State the blood parasite species.
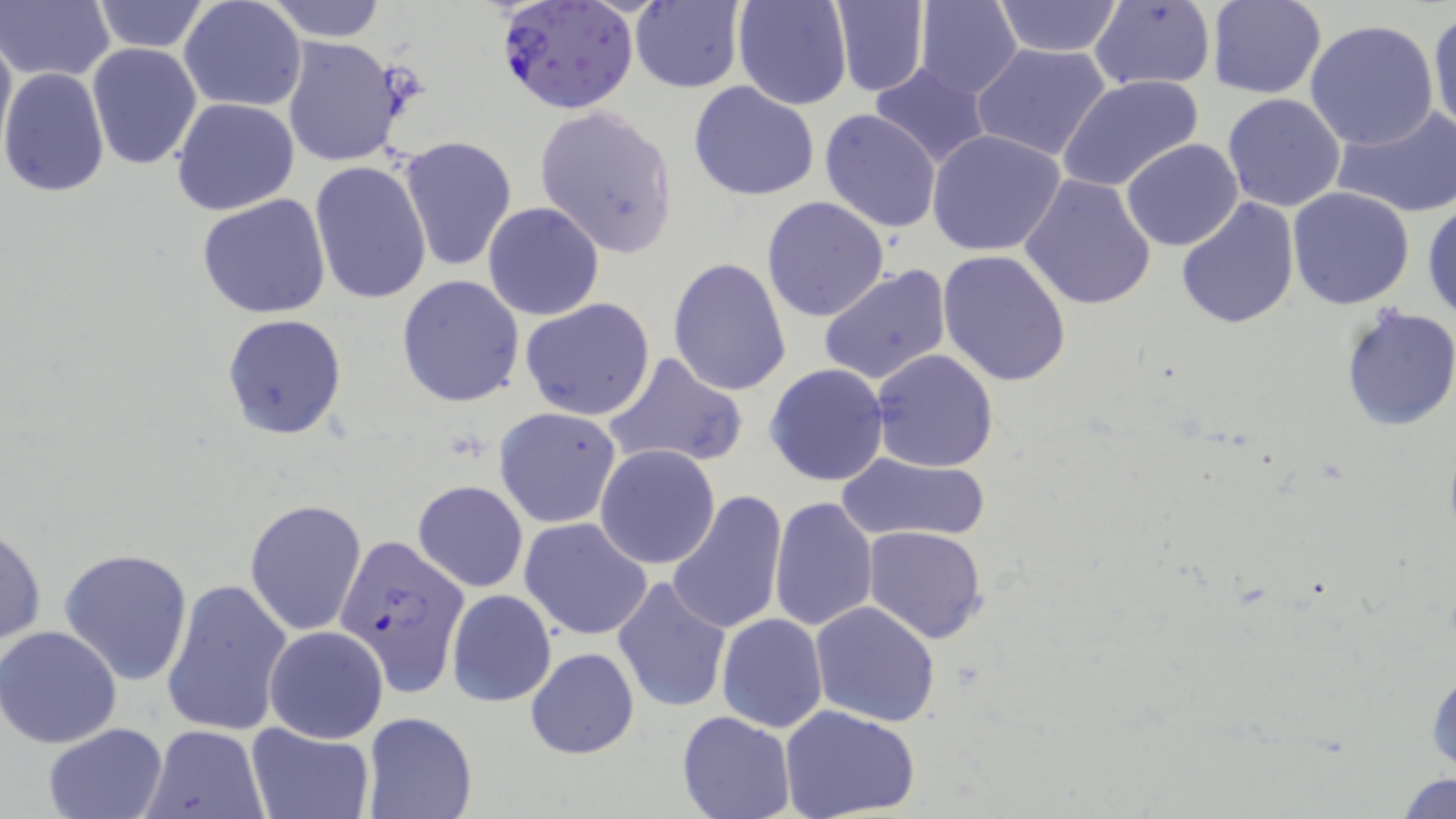

Plasmodium falciparum.

Summary:
  - Coordinate format: approximate bounding boxes as [x1, y1, x2, y2] in pixels
  - Plasmodium falciparum-infected red blood cell locations: [495, 0, 641, 116], [334, 537, 470, 700]
  - Uninfected red blood cell locations: [88, 0, 213, 54], [178, 0, 307, 112], [261, 0, 389, 41], [731, 0, 852, 109], [913, 0, 1022, 98], [630, 1, 745, 93], [831, 1, 931, 95], [992, 1, 1124, 56], [1205, 1, 1328, 100], [1, 2, 114, 83], [1087, 2, 1217, 91], [854, 3, 1008, 139], [1428, 8, 1456, 139], [1302, 19, 1439, 152], [0, 23, 15, 160], [281, 35, 414, 168], [86, 42, 203, 171], [970, 43, 1114, 163], [869, 62, 991, 167], [0, 66, 112, 197], [1057, 74, 1205, 193], [688, 82, 821, 201], [1221, 91, 1346, 211], [170, 97, 299, 215], [533, 104, 679, 258], [1331, 106, 1456, 219], [819, 108, 942, 231], [927, 129, 1066, 256], [397, 135, 517, 272], [1121, 139, 1245, 252], [308, 161, 432, 305], [1020, 174, 1157, 309], [1286, 187, 1415, 311], [197, 194, 333, 318], [761, 196, 889, 323], [1175, 196, 1301, 331], [1422, 198, 1456, 324], [482, 200, 604, 321], [938, 251, 1072, 388], [667, 257, 793, 397], [818, 266, 952, 388], [397, 274, 524, 407], [520, 298, 655, 422], [1339, 307, 1456, 432], [221, 313, 347, 440], [870, 348, 999, 472], [602, 350, 749, 471], [764, 363, 890, 486], [494, 407, 622, 528], [595, 444, 720, 569], [836, 451, 992, 544], [413, 480, 528, 593], [665, 490, 786, 635], [769, 495, 879, 632], [245, 498, 367, 636], [520, 517, 654, 640], [0, 522, 46, 651], [863, 527, 986, 644], [58, 547, 195, 686], [612, 575, 732, 714], [162, 577, 293, 739], [446, 589, 556, 707], [809, 600, 940, 727], [717, 614, 827, 731], [0, 626, 122, 748], [264, 626, 388, 743], [524, 647, 642, 759], [1425, 658, 1455, 778], [780, 706, 920, 819], [676, 709, 796, 819], [363, 713, 477, 819], [248, 722, 373, 818], [41, 723, 167, 819], [140, 725, 268, 818], [1395, 772, 1455, 817]
  - Magnification: 1000x
  - Preparation: thin blood smear
  - Modality: optical microscopy
  - Image size: 1456×819 pixels
  - Stain: May-Grünwald-Giemsa
  - Field of view: single